Assess this cell for malaria.
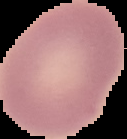

Uninfected.

From a thin blood film. Image is 127×139 pixels. Cell region segmented out of the field of view; the surrounding area is masked to black.